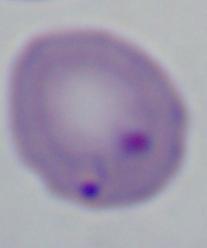
magnification = 1000x
identification = Babesia
modality = micrograph